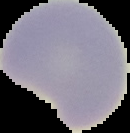
image type = cell region segmented out of the field of view; surrounding area masked to black
preparation = thin blood film
result = negative for malaria parasites
image size = 130×133 pixels